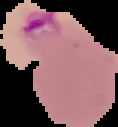 From a thin blood smear. Segmented cell region on a black background. Image is 118×127 pixels. Malaria status: parasitized.